Rate the background quality.
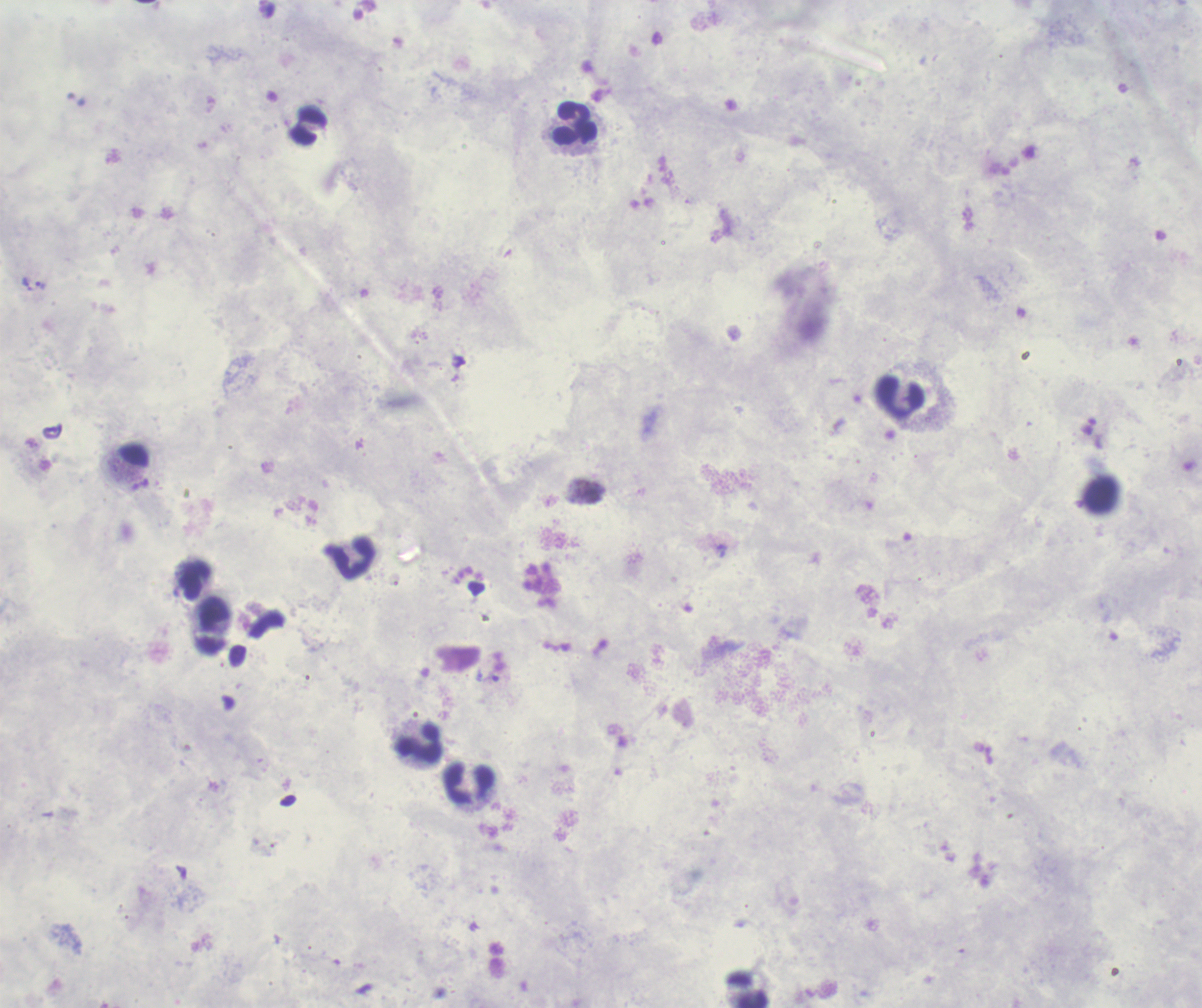

Poor.

{
  "image_size": "1202×1008 pixels",
  "result": "positive for Plasmodium parasites",
  "preparation": "thick smear of blood",
  "magnification": "100x",
  "trophozoite_locations": "approximate centers as {x, y} in pixels: {41, 285}",
  "field_of_view": "single",
  "context": "previously used in a real diagnosis",
  "stain": "Romanowsky",
  "leukocyte_locations": "approximate centers as {x, y} in pixels: {575, 123}, {900, 399}, {351, 558}, {194, 580}, {420, 744}, {468, 785}"
}